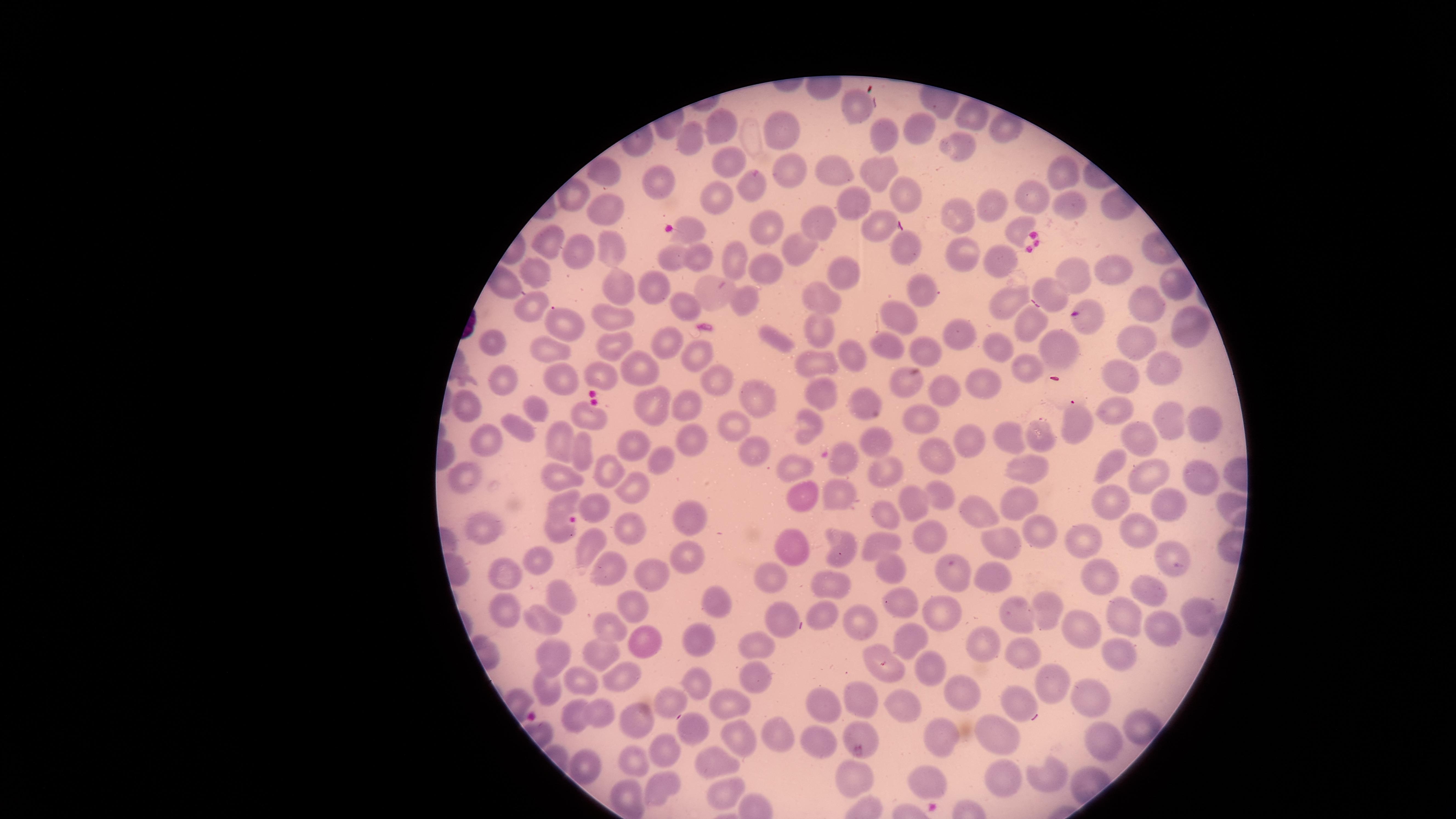
Approximate marker points as (x, y) in pixels. Uninfected red blood cells: (857, 101), (969, 107), (716, 121), (927, 126), (786, 130), (1002, 131), (688, 137), (878, 138), (962, 143), (725, 158), (830, 172), (1065, 172), (607, 173), (657, 174), (872, 174), (792, 177), (905, 193), (1031, 195), (851, 203), (1061, 206), (993, 207), (711, 208), (609, 209), (952, 216), (876, 223), (755, 224), (821, 226), (1014, 226), (689, 232), (902, 242), (607, 245), (791, 248), (552, 249), (588, 250), (695, 250), (959, 252), (674, 255), (735, 259), (999, 264), (1115, 268), (538, 270), (767, 272), (1069, 272), (842, 275), (1173, 283), (501, 285), (655, 287), (921, 287), (628, 288), (1045, 288), (721, 292), (688, 297), (749, 298), (830, 300), (1005, 302), (1149, 304), (532, 310), (903, 319), (561, 321), (608, 321), (1033, 321), (1090, 322), (1192, 325), (822, 334), (960, 335), (1126, 335), (776, 338), (887, 339), (486, 341), (997, 342), (668, 343), (612, 344), (1055, 346), (549, 348), (928, 350), (856, 351), (696, 353), (821, 364), (1162, 365), (1033, 368), (644, 371), (1121, 373), (599, 374), (715, 374), (501, 378), (559, 378), (979, 379), (902, 381), (822, 390), (939, 390), (751, 392), (691, 402), (863, 405), (463, 407), (647, 409), (1111, 409), (534, 410), (1165, 418), (919, 419), (1203, 419), (583, 420), (517, 425), (1074, 425), (729, 426), (810, 429), (1037, 434), (1008, 435), (875, 437), (490, 439), (1138, 439), (690, 440), (966, 440), (561, 442), (635, 444), (759, 449), (582, 451), (660, 457), (946, 458), (794, 463), (848, 465), (1110, 465), (458, 466), (1023, 466), (881, 470), (1149, 470), (1201, 472), (552, 473), (604, 476), (630, 487), (800, 493), (938, 493), (838, 497), (1113, 498), (562, 502), (1019, 505), (599, 507), (912, 507), (1165, 508), (979, 512), (693, 513), (890, 515), (553, 525), (1138, 525), (629, 527), (1037, 530), (490, 531), (927, 542), (882, 543), (1081, 543), (592, 547), (792, 548), (838, 548), (998, 548), (1167, 553), (536, 554), (688, 554), (608, 566), (505, 569), (652, 571), (888, 571), (957, 571), (989, 574), (1094, 577), (767, 581), (1149, 586), (827, 587), (553, 591), (905, 601), (629, 603), (500, 606), (716, 606), (1017, 607), (1048, 608), (820, 609), (1124, 613), (861, 614), (943, 614), (1196, 615), (542, 617), (782, 620), (612, 622), (1160, 623), (1086, 630), (696, 637), (913, 639), (643, 642), (983, 643), (755, 648), (556, 651), (604, 652), (1024, 652), (870, 653), (1114, 658), (927, 665), (749, 675), (579, 677), (622, 679), (544, 681), (698, 683), (1053, 683), (967, 693), (1010, 695), (664, 696), (865, 700), (1086, 700), (822, 703), (907, 706), (728, 709), (598, 710), (574, 713), (638, 724), (1139, 725), (688, 726), (862, 729), (780, 733), (999, 735), (936, 736), (739, 740), (820, 740), (1108, 740), (669, 753), (633, 755), (579, 761), (715, 767), (1002, 772), (856, 775), (1044, 779), (926, 784), (660, 786), (719, 791), (622, 794). Circular visible region. Presence: no malaria parasites identified. Image is 1456×819 pixels. Giemsa-stained preparation. Single field of view. Thin blood film. Smartphone photograph through the microscope eyepiece.